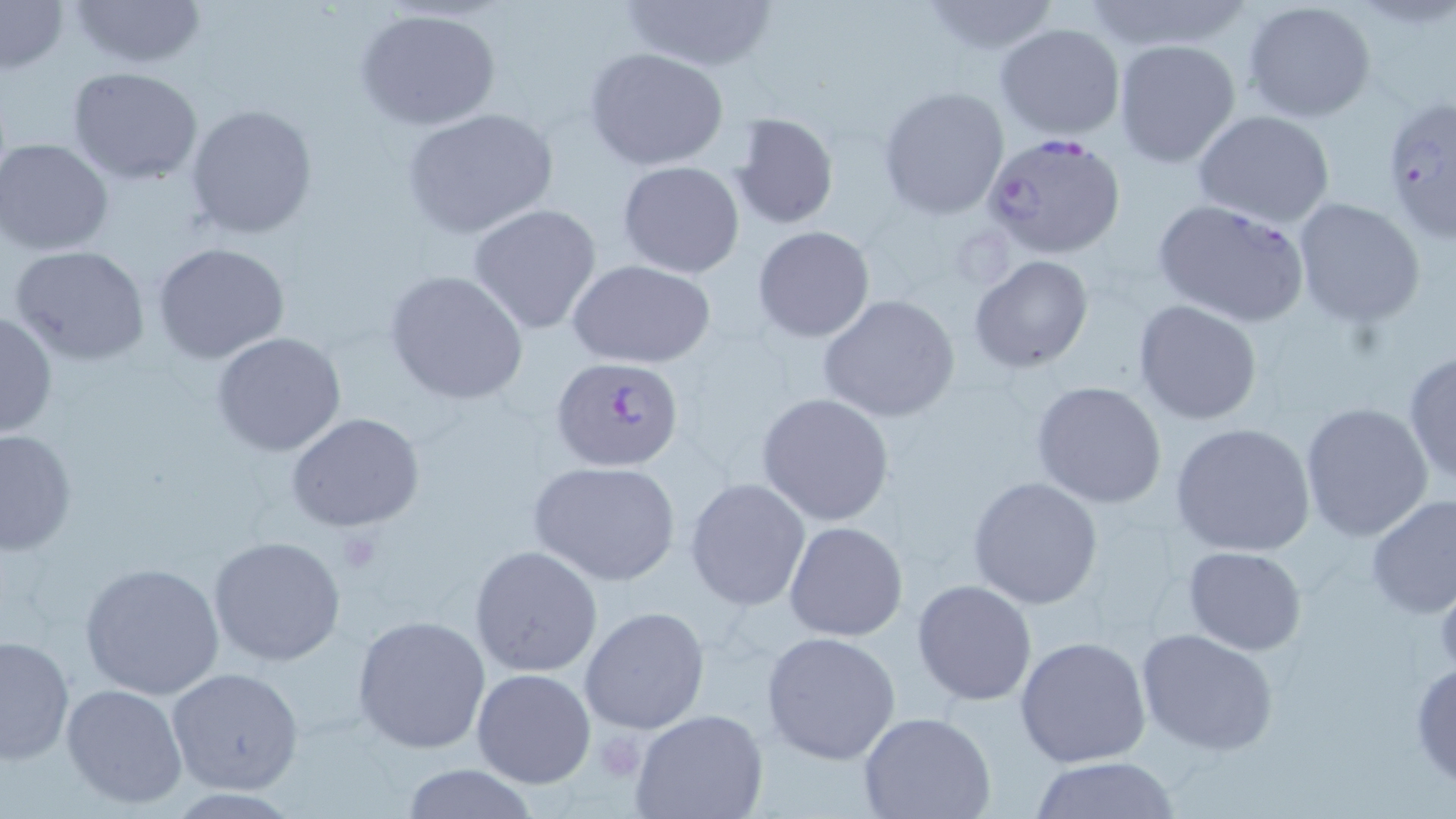

Plasmodium falciparum-infected red blood cell locations = approximate bounding boxes as (x1, y1, x2, y2) in pixels: (1381, 91, 1455, 245), (985, 135, 1130, 263), (1151, 198, 1312, 328), (552, 355, 685, 473)
slide-level diagnosis = Plasmodium falciparum
stain = May-Grünwald-Giemsa
preparation = thin blood film
platelet locations = approximate bounding boxes as (x1, y1, x2, y2) in pixels: (334, 529, 385, 575), (1432, 571, 1456, 680), (592, 733, 644, 781)
modality = optical microscopy
image size = 1456×819 pixels
field of view = one of a larger specimen
magnification = 1000x
uninfected red blood cell locations = approximate bounding boxes as (x1, y1, x2, y2) in pixels: (64, 0, 205, 70), (615, 0, 782, 71), (918, 0, 1064, 56), (1242, 0, 1377, 123), (0, 1, 69, 76), (353, 7, 501, 132), (994, 21, 1126, 141), (1113, 40, 1242, 169), (585, 47, 730, 170), (68, 65, 202, 185), (877, 86, 1009, 220), (185, 103, 317, 240), (401, 107, 560, 238), (1192, 109, 1336, 227), (729, 111, 839, 231), (1, 138, 116, 255), (616, 161, 744, 278), (1291, 198, 1427, 325), (468, 203, 602, 335), (752, 226, 875, 343), (152, 241, 290, 364), (8, 245, 153, 367), (968, 255, 1095, 372), (568, 259, 717, 369), (384, 270, 528, 404), (818, 295, 960, 424), (1132, 300, 1263, 426), (0, 309, 57, 441), (211, 332, 348, 457), (1402, 351, 1456, 488), (1030, 380, 1167, 510), (757, 393, 894, 526), (1300, 401, 1434, 543), (285, 411, 423, 532), (1169, 422, 1318, 558), (1, 429, 76, 557), (528, 460, 683, 586), (685, 477, 812, 612), (968, 477, 1103, 610), (1365, 493, 1456, 622), (783, 521, 908, 642), (208, 535, 346, 667), (469, 545, 604, 678), (1182, 546, 1308, 654), (78, 561, 226, 701), (913, 580, 1037, 704), (579, 607, 710, 735), (352, 615, 490, 752), (1136, 628, 1281, 756), (759, 630, 903, 765), (0, 634, 74, 766), (1013, 635, 1152, 768), (1409, 660, 1456, 787), (167, 667, 306, 796), (471, 669, 596, 789), (60, 683, 188, 810), (630, 707, 768, 819), (860, 713, 996, 819), (1025, 757, 1186, 817), (395, 764, 544, 819)